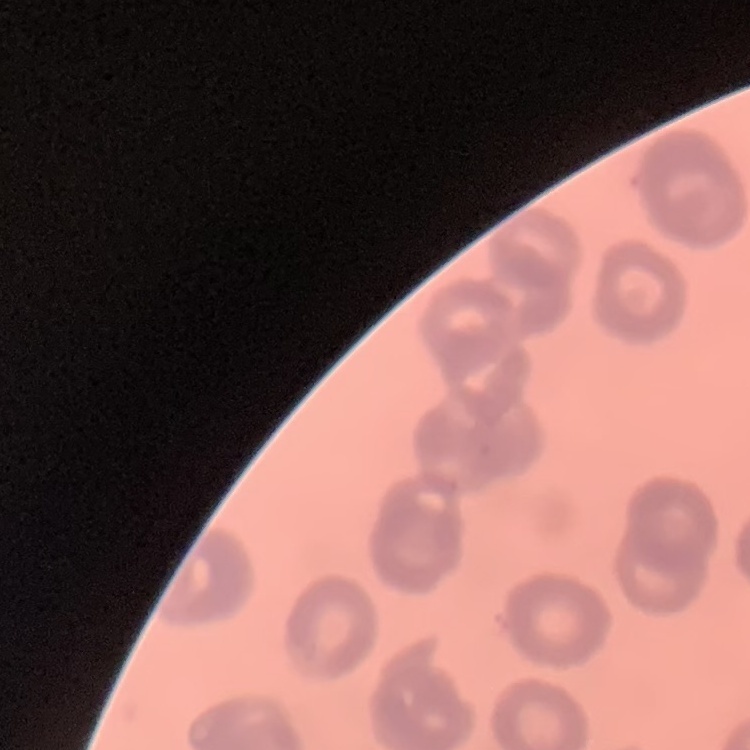
The red blood cells exhibit rouleaux formation. Field's or Giemsa stain. Square crop of a larger photomicrograph. Thin blood film.